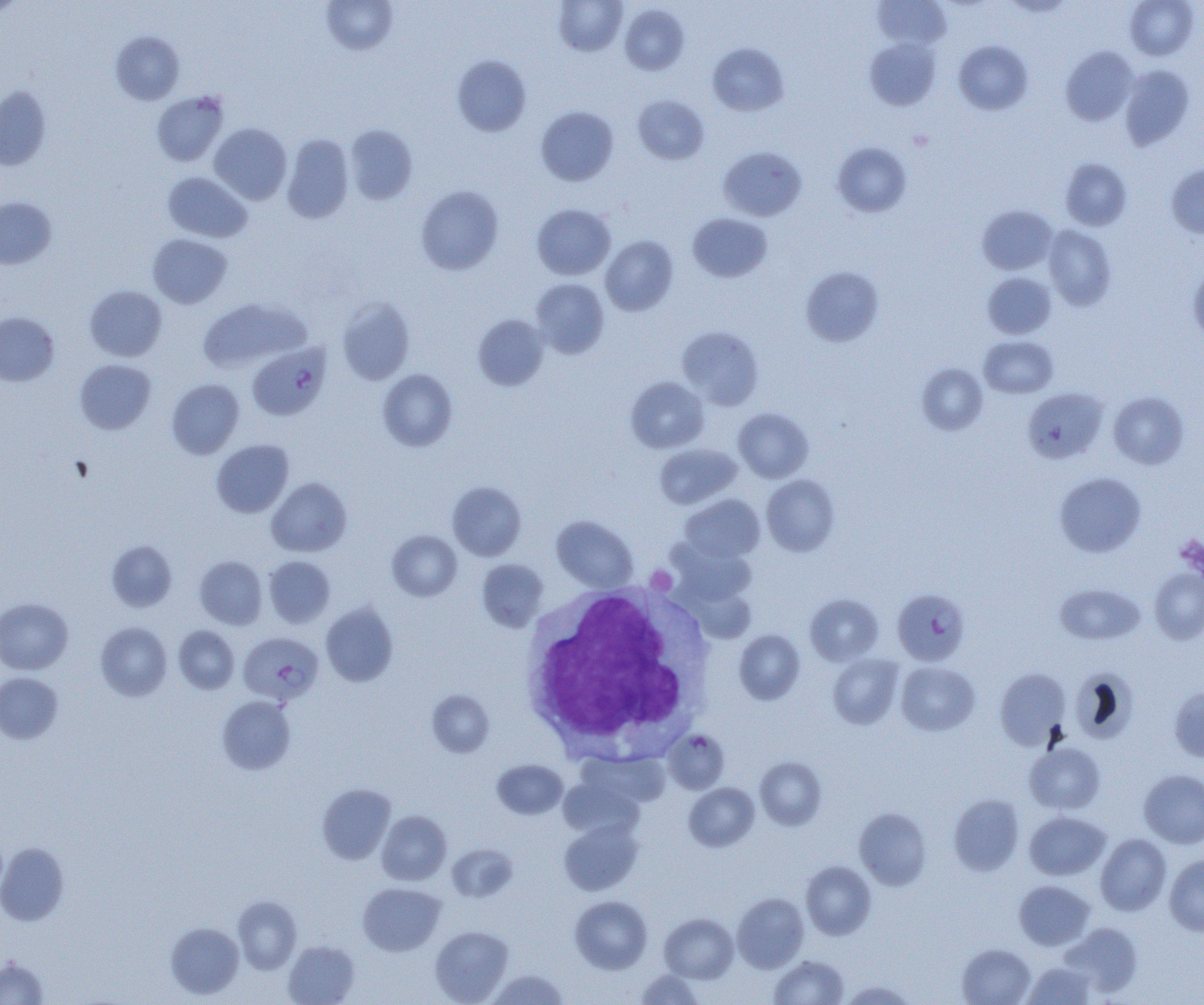 Approximate bounding boxes as [x1, y1, x2, y2] in pixels. Platelet locations: [1175, 534, 1204, 579], [646, 566, 677, 594]. Plasmodium falciparum-infected red blood cell locations: [248, 344, 330, 421], [892, 588, 970, 665], [238, 632, 323, 705], [664, 729, 730, 794]. White blood cell locations: [520, 582, 715, 757]. Uninfected red blood cell locations: [321, 0, 398, 55], [553, 0, 627, 56], [873, 0, 951, 49], [1124, 0, 1199, 60], [0, 1, 26, 18], [620, 4, 689, 75], [110, 31, 185, 105], [864, 37, 941, 110], [953, 40, 1032, 115], [708, 42, 789, 116], [1060, 46, 1138, 125], [452, 54, 531, 136], [1120, 65, 1195, 149], [0, 86, 51, 170], [151, 91, 229, 166], [633, 95, 710, 164], [536, 106, 619, 186], [209, 123, 292, 204], [345, 124, 418, 205], [282, 134, 353, 223], [832, 142, 912, 217], [718, 146, 807, 221], [1060, 158, 1132, 230], [1166, 164, 1204, 239], [162, 171, 252, 243], [416, 185, 504, 275], [0, 197, 57, 269], [531, 203, 616, 280], [977, 204, 1057, 274], [688, 212, 772, 282], [1043, 224, 1116, 311], [148, 234, 232, 308], [600, 235, 678, 316], [1188, 264, 1204, 345], [800, 266, 884, 346], [982, 272, 1056, 339], [529, 278, 609, 359], [84, 285, 167, 361], [198, 297, 310, 373], [336, 297, 416, 384], [0, 312, 59, 386], [473, 313, 550, 390], [677, 326, 764, 410], [979, 335, 1058, 398], [75, 359, 156, 434], [916, 363, 988, 435], [377, 369, 457, 451], [626, 376, 709, 452], [167, 379, 244, 459], [1022, 387, 1108, 464], [1109, 391, 1189, 469], [734, 407, 813, 483], [211, 440, 293, 518], [654, 443, 742, 510], [1054, 472, 1146, 557], [761, 474, 840, 556], [267, 477, 352, 557], [447, 481, 526, 561], [679, 495, 765, 563], [552, 516, 638, 591], [387, 530, 462, 601], [106, 540, 177, 612], [670, 543, 755, 607], [194, 556, 267, 629], [263, 556, 335, 628], [477, 559, 549, 632], [1149, 568, 1204, 644], [1055, 583, 1146, 645], [685, 585, 757, 643], [804, 594, 884, 666], [0, 597, 73, 674], [320, 603, 398, 687], [95, 622, 172, 701], [173, 626, 239, 694], [734, 630, 805, 704], [828, 654, 904, 729], [896, 661, 980, 736], [994, 667, 1069, 749], [1070, 668, 1139, 744], [0, 672, 63, 744], [1169, 686, 1204, 763], [427, 689, 495, 757], [217, 695, 296, 775], [1025, 741, 1106, 814], [755, 757, 827, 830], [492, 759, 568, 820], [1138, 769, 1204, 848], [559, 777, 645, 840], [317, 783, 396, 865], [684, 783, 759, 851], [949, 794, 1024, 876], [854, 807, 932, 890], [377, 811, 451, 885], [1024, 811, 1111, 880], [559, 819, 643, 896], [1095, 834, 1172, 916], [0, 843, 69, 926], [446, 844, 518, 902], [1164, 855, 1204, 936], [801, 861, 876, 939], [1014, 880, 1095, 950], [358, 882, 446, 956], [731, 893, 809, 972], [570, 895, 652, 973], [233, 896, 302, 973], [659, 913, 738, 983], [166, 922, 244, 999], [1060, 922, 1143, 997], [430, 925, 513, 1004], [283, 940, 360, 1005], [957, 943, 1036, 1005], [769, 955, 849, 1005], [0, 957, 50, 1005], [1023, 961, 1097, 1004], [486, 969, 569, 1004], [635, 969, 704, 1004], [840, 980, 917, 1005]. Slide-level diagnosis: Plasmodium falciparum. Thin blood smear. Single field of view. Light microscopy. 1000x magnification. Image is 1204×1005 pixels.